Outline each uninfected red blood cell.
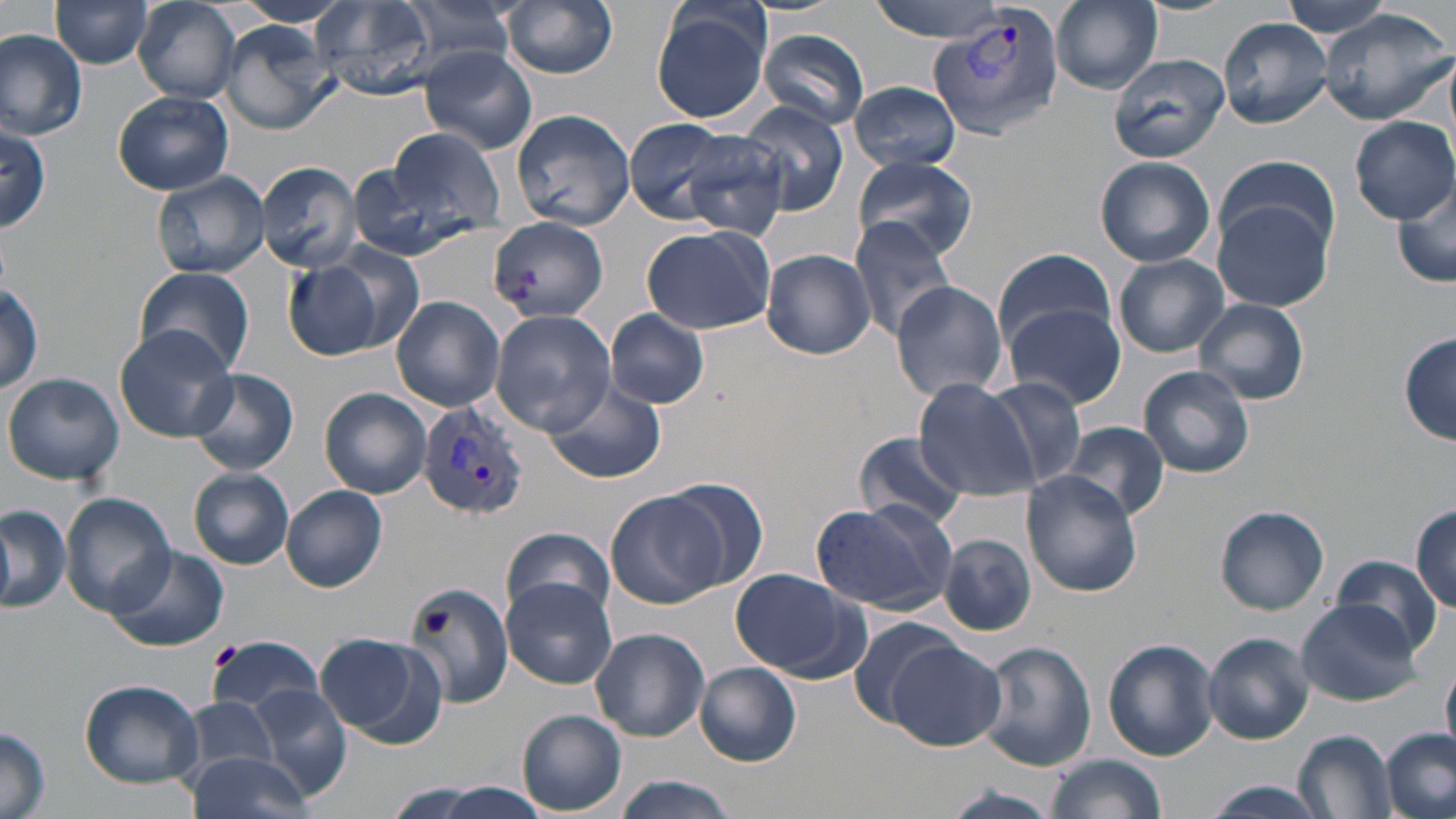
Approximate bounding boxes as [x1, y1, x2, y2] in pixels.
Uninfected red blood cells: [49, 0, 155, 67], [233, 0, 353, 27], [394, 0, 524, 65], [503, 0, 620, 77], [649, 0, 774, 122], [866, 0, 1018, 40], [1051, 0, 1164, 93], [1282, 0, 1396, 39], [133, 1, 243, 103], [311, 1, 441, 101], [1317, 9, 1454, 125], [1218, 17, 1333, 129], [216, 20, 337, 135], [757, 29, 871, 130], [0, 30, 88, 139], [417, 46, 539, 156], [1107, 53, 1230, 163], [850, 80, 963, 170], [112, 91, 234, 195], [740, 103, 849, 217], [511, 108, 634, 231], [1350, 116, 1455, 222], [622, 117, 739, 223], [0, 125, 49, 232], [383, 125, 505, 235], [679, 128, 792, 241], [1213, 155, 1342, 254], [851, 156, 979, 261], [1094, 156, 1217, 267], [349, 157, 486, 262], [255, 161, 361, 273], [152, 173, 268, 278], [1392, 180, 1456, 289], [1210, 200, 1336, 313], [487, 218, 610, 323], [848, 218, 957, 340], [641, 224, 776, 335], [321, 242, 425, 353], [993, 247, 1117, 350], [763, 249, 875, 359], [1113, 254, 1230, 357], [285, 262, 384, 359], [133, 266, 257, 376], [0, 281, 43, 393], [890, 281, 1009, 401], [391, 295, 505, 412], [1193, 298, 1309, 404], [1002, 302, 1126, 409], [606, 309, 710, 409], [491, 310, 616, 435], [115, 323, 239, 444], [1399, 332, 1456, 445], [1139, 366, 1255, 477], [190, 367, 298, 475], [4, 372, 124, 486], [541, 376, 666, 485], [913, 377, 1036, 499], [987, 377, 1086, 489], [319, 388, 433, 499], [1062, 422, 1170, 522], [853, 430, 970, 528], [189, 469, 294, 570], [1022, 469, 1145, 597], [663, 477, 767, 591], [281, 485, 387, 593], [62, 493, 176, 619], [605, 494, 726, 609], [809, 498, 959, 614], [1412, 504, 1455, 612], [1215, 505, 1330, 615], [0, 507, 71, 613], [1387, 523, 1456, 643], [501, 526, 614, 625], [938, 533, 1037, 637], [107, 545, 228, 653], [1328, 554, 1444, 657], [729, 567, 862, 679], [404, 577, 518, 710], [501, 577, 615, 689], [1297, 598, 1428, 708], [845, 616, 963, 727], [590, 627, 709, 742], [318, 632, 446, 748], [1204, 632, 1314, 744], [205, 635, 325, 716], [1102, 638, 1220, 761], [885, 641, 1005, 750], [979, 641, 1095, 771], [695, 663, 801, 765], [1442, 665, 1456, 757], [80, 679, 205, 787], [248, 689, 352, 801], [180, 698, 282, 780], [517, 710, 626, 814], [0, 724, 51, 819], [1382, 728, 1455, 819], [1295, 731, 1398, 817], [187, 749, 316, 819], [1041, 752, 1166, 819], [611, 776, 739, 818], [1191, 781, 1332, 818], [413, 782, 553, 819], [939, 787, 1062, 819].

Summary:
  - Plasmodium vivax-infected red blood cell locations: [926, 8, 1065, 142], [417, 400, 529, 523]
  - Slide-level diagnosis: Plasmodium vivax
  - Modality: light microscopy
  - Field of view: single
  - Magnification: 1000x
  - Stain: May-Grünwald-Giemsa
  - Preparation: thin blood smear
  - Image size: 1456×819 pixels